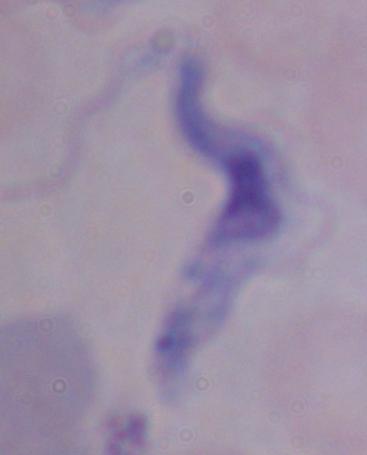
identification = trypanosome
modality = photomicrograph
magnification = 1000x